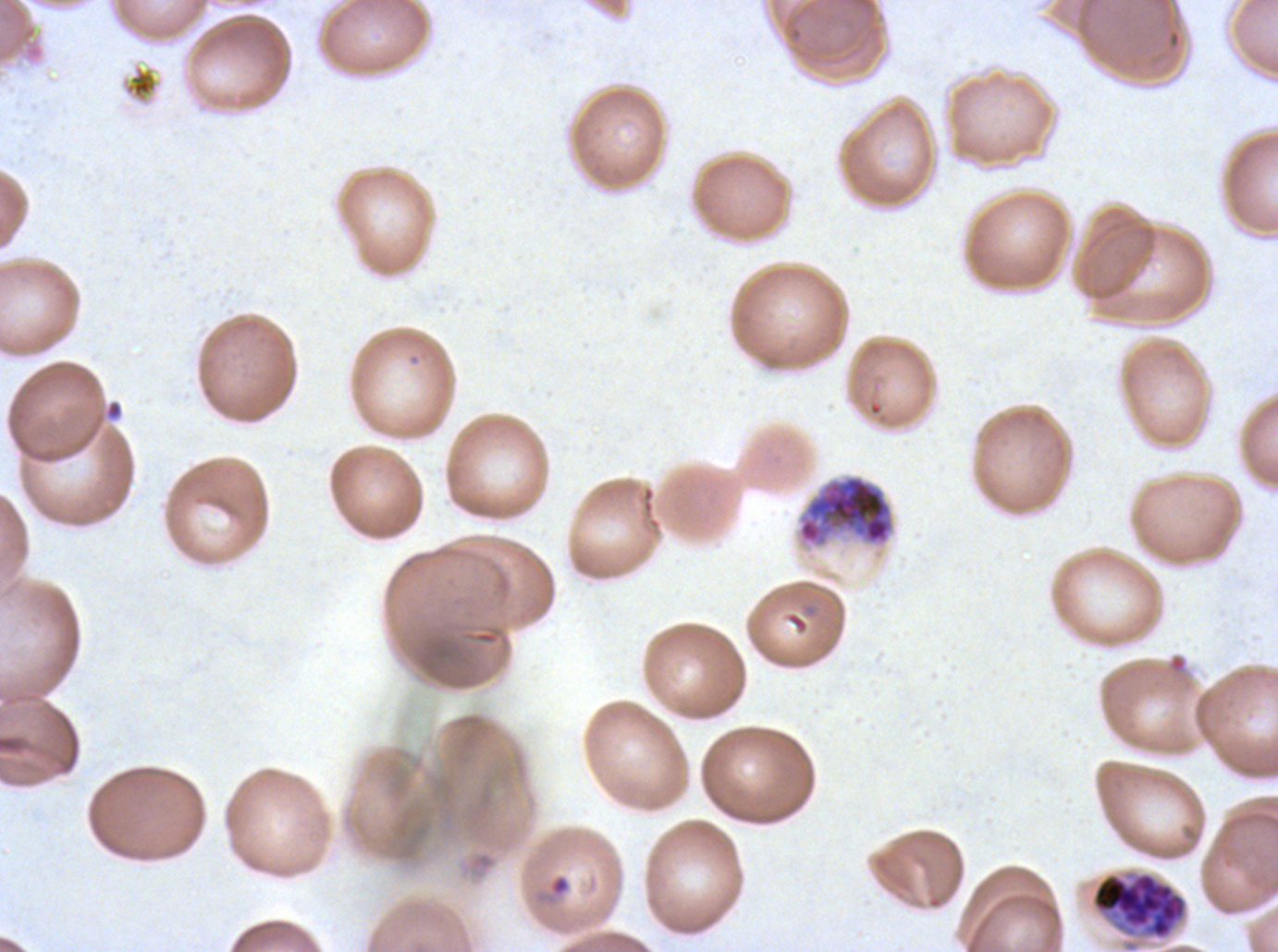 Approximate bounding boxes as (x1, y1, x2, y2) in pixels. Early schizont locations: (797, 474, 895, 547). Ring locations: (104, 399, 124, 421), (549, 874, 571, 897). Debris locations: (0, 0, 45, 65). Late schizont locations: (1091, 871, 1187, 940). Plasmodium falciparum from a patient in The Gambia, cultured ex vivo for 24 to 48 hours. Image is 1278×952 pixels. One sub-image of a larger composite. Life-cycle stages observed: ring, early schizont, late schizont. Giemsa stain. Thin blood film.